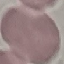
result = no malaria parasites detected
image type = cell patch, automatically extracted from a larger field of view and resized to 64 × 64 pixels
capture = smartphone camera at the microscope eyepiece
preparation = thin smear
stain = Giemsa